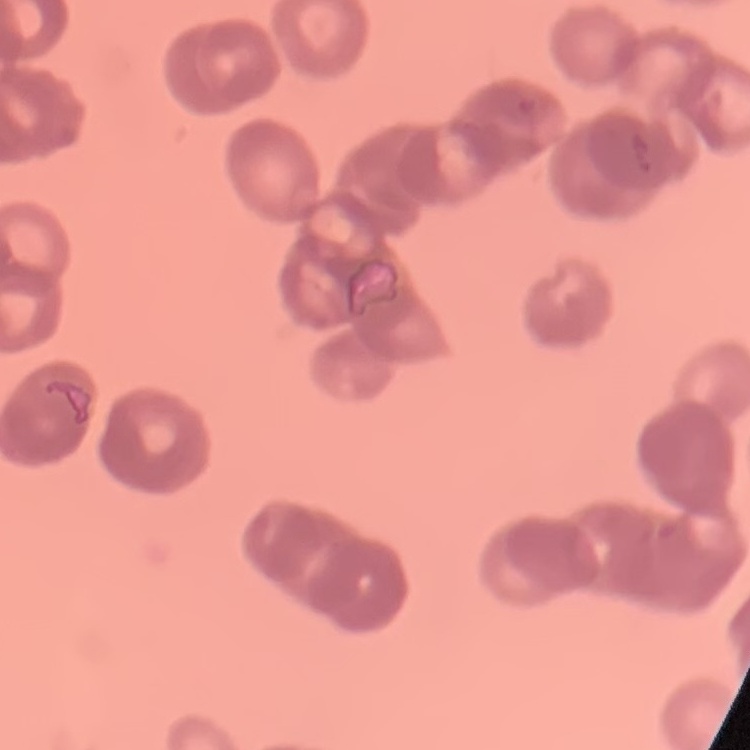
Summary:
  - Erythrocyte morphology: rouleaux formation
  - Image type: one tile cut from a larger photomicrograph
  - Preparation: thin peripheral smear
  - Stain: Field's or Giemsa